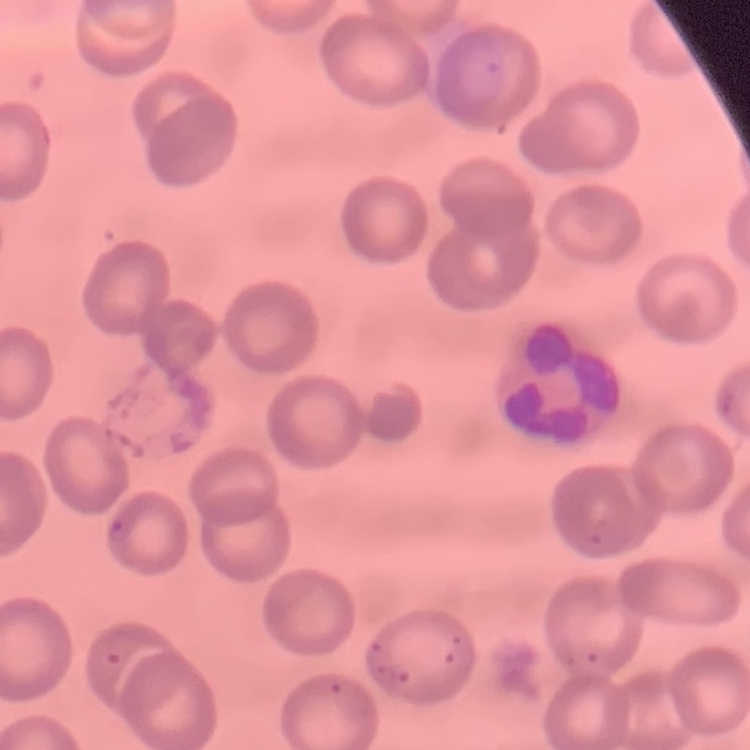
erythrocyte morphology = no rouleaux formation
image type = square crop of a larger photomicrograph
preparation = thin blood film
stain = Field's or Giemsa